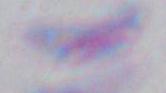

magnification: 1000x
modality: photomicrograph
identification: Toxoplasma gondii